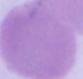

A red blood cell is shown. Captured at 1000x magnification. Photomicrograph.